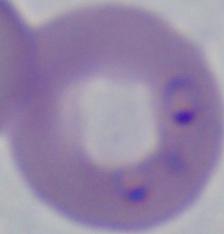

Micrograph. A Babesia parasite is shown. Captured at 1000x magnification.